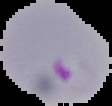
Summary:
  - Result: Plasmodium parasites detected
  - Image size: 112×106 pixels
  - Preparation: thin blood smear
  - Image type: segmented cell region on a black background